Locate every blood parasite and identify its species.
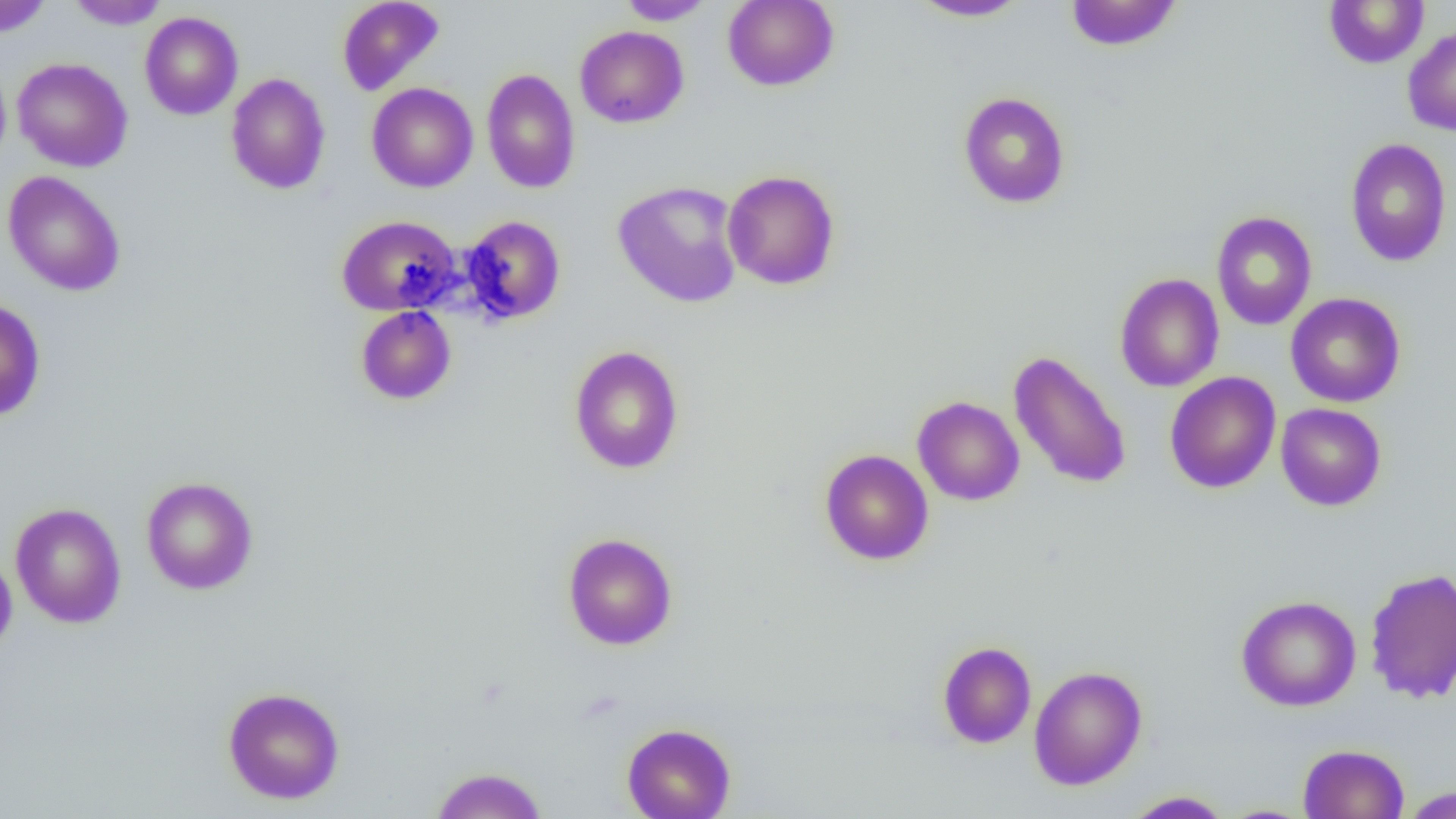
No blood parasites observed.

Summary:
  - Coordinate format: approximate bounding boxes as named x1/y1/x2/y2 corners in pixels
  - Uninfected red blood cell locations: (x1=0, y1=0, x2=54, y2=37), (x1=65, y1=0, x2=170, y2=29), (x1=336, y1=0, x2=444, y2=96), (x1=617, y1=0, x2=716, y2=25), (x1=722, y1=0, x2=839, y2=92), (x1=907, y1=0, x2=1033, y2=22), (x1=1064, y1=0, x2=1183, y2=52), (x1=1323, y1=0, x2=1429, y2=68), (x1=140, y1=11, x2=243, y2=120), (x1=575, y1=25, x2=689, y2=128), (x1=1403, y1=26, x2=1456, y2=136), (x1=12, y1=57, x2=133, y2=172), (x1=0, y1=62, x2=12, y2=172), (x1=481, y1=68, x2=581, y2=194), (x1=226, y1=72, x2=331, y2=194), (x1=366, y1=82, x2=478, y2=193), (x1=958, y1=91, x2=1070, y2=209), (x1=1345, y1=138, x2=1452, y2=266), (x1=722, y1=169, x2=840, y2=290), (x1=2, y1=170, x2=126, y2=296), (x1=612, y1=180, x2=744, y2=308), (x1=1212, y1=212, x2=1317, y2=331), (x1=336, y1=214, x2=461, y2=315), (x1=461, y1=215, x2=566, y2=324), (x1=1114, y1=273, x2=1224, y2=392), (x1=1286, y1=292, x2=1405, y2=408), (x1=0, y1=297, x2=46, y2=421), (x1=355, y1=306, x2=456, y2=405), (x1=569, y1=345, x2=684, y2=474), (x1=1008, y1=350, x2=1131, y2=490), (x1=1165, y1=371, x2=1281, y2=494), (x1=912, y1=396, x2=1025, y2=506), (x1=1276, y1=403, x2=1386, y2=511), (x1=819, y1=449, x2=934, y2=565), (x1=141, y1=477, x2=258, y2=595), (x1=10, y1=503, x2=127, y2=628), (x1=563, y1=532, x2=678, y2=650), (x1=0, y1=551, x2=17, y2=660), (x1=1364, y1=568, x2=1456, y2=704), (x1=1235, y1=595, x2=1361, y2=711), (x1=937, y1=641, x2=1036, y2=748), (x1=1029, y1=665, x2=1147, y2=790), (x1=222, y1=686, x2=345, y2=805), (x1=622, y1=723, x2=736, y2=819), (x1=1298, y1=743, x2=1410, y2=819), (x1=430, y1=767, x2=547, y2=819), (x1=1400, y1=786, x2=1454, y2=818), (x1=1123, y1=790, x2=1232, y2=818), (x1=1217, y1=804, x2=1316, y2=818)
  - Slide-level diagnosis: negative for blood parasites
  - Field of view: single
  - Modality: optical microscopy
  - Preparation: thin blood film
  - Magnification: 1000x
  - Image size: 1456×819 pixels